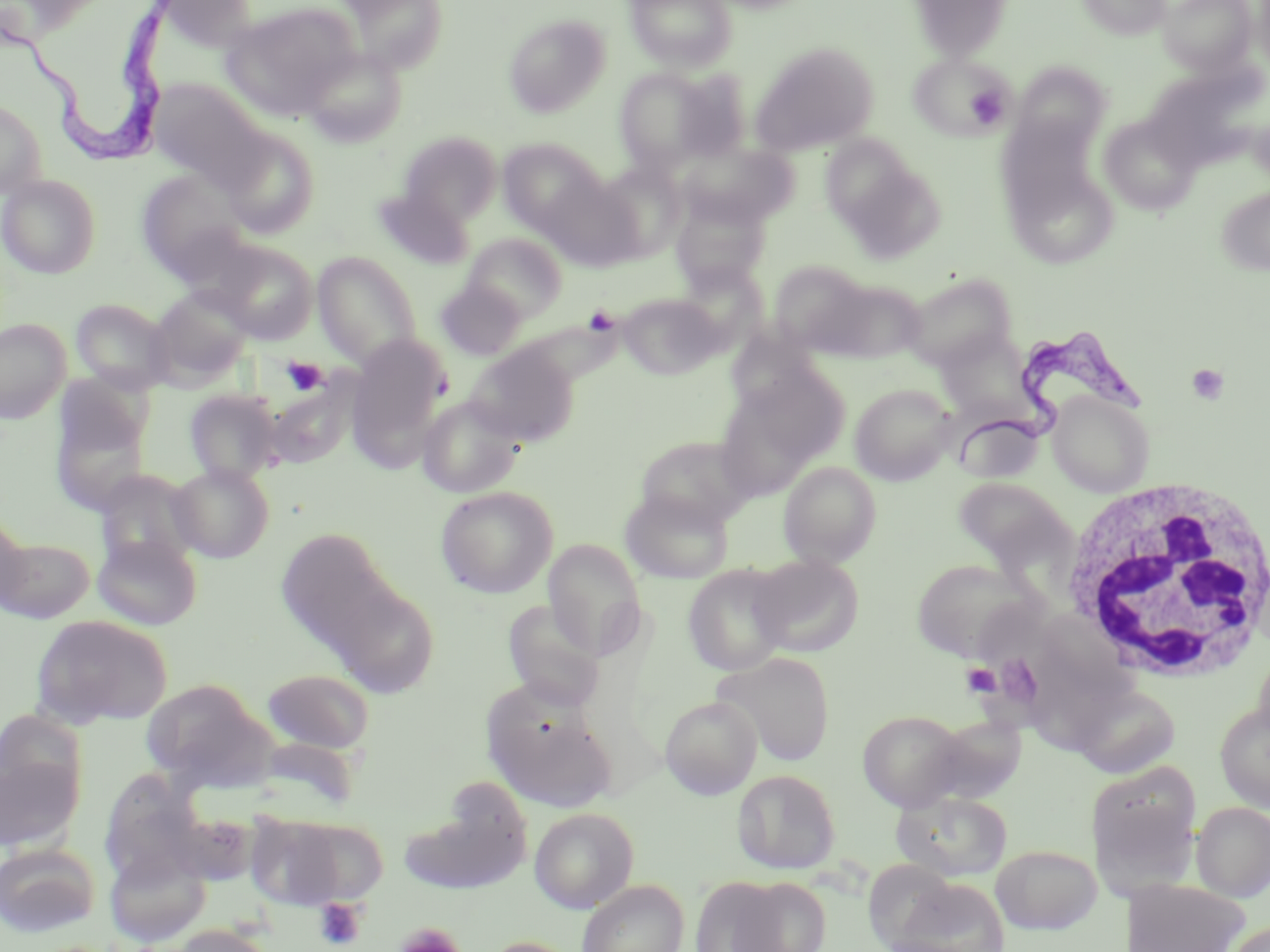

{
  "slide_level_diagnosis": "Trypanosoma brucei",
  "image_size": "1270×952 pixels",
  "trypanosoma_brucei_locations": "approximate bounding boxes as named x1/y1/x2/y2 corners in pixels: (x1=0, y1=1, x2=177, y2=155), (x1=956, y1=328, x2=1147, y2=465)",
  "modality": "optical microscopy",
  "preparation": "thin blood smear",
  "platelet_locations": "approximate bounding boxes as named x1/y1/x2/y2 corners in pixels: (x1=965, y1=85, x2=1007, y2=128), (x1=282, y1=357, x2=328, y2=395), (x1=1186, y1=363, x2=1229, y2=405), (x1=961, y1=663, x2=1000, y2=697), (x1=313, y1=898, x2=367, y2=950), (x1=397, y1=923, x2=463, y2=952)",
  "uninfected_red_blood_cell_locations": "approximate bounding boxes as named x1/y1/x2/y2 corners in pixels: (x1=150, y1=0, x2=258, y2=48), (x1=343, y1=0, x2=449, y2=73), (x1=624, y1=0, x2=738, y2=71), (x1=909, y1=0, x2=1014, y2=61), (x1=1077, y1=0, x2=1171, y2=39), (x1=1159, y1=0, x2=1256, y2=75), (x1=1252, y1=0, x2=1270, y2=76), (x1=221, y1=2, x2=360, y2=120), (x1=504, y1=15, x2=610, y2=117), (x1=751, y1=41, x2=880, y2=155), (x1=301, y1=48, x2=407, y2=147), (x1=911, y1=53, x2=1012, y2=139), (x1=1012, y1=62, x2=1113, y2=154), (x1=614, y1=68, x2=721, y2=173), (x1=671, y1=69, x2=753, y2=162), (x1=148, y1=78, x2=269, y2=187), (x1=0, y1=97, x2=47, y2=199), (x1=1099, y1=114, x2=1202, y2=216), (x1=1250, y1=115, x2=1270, y2=183), (x1=994, y1=116, x2=1108, y2=230), (x1=219, y1=129, x2=320, y2=238), (x1=399, y1=131, x2=502, y2=226), (x1=819, y1=134, x2=923, y2=233), (x1=497, y1=138, x2=605, y2=234), (x1=677, y1=141, x2=796, y2=229), (x1=595, y1=160, x2=688, y2=260), (x1=135, y1=169, x2=251, y2=279), (x1=0, y1=174, x2=101, y2=279), (x1=540, y1=175, x2=643, y2=271), (x1=1014, y1=181, x2=1117, y2=272), (x1=1216, y1=185, x2=1270, y2=275), (x1=373, y1=187, x2=473, y2=270), (x1=671, y1=194, x2=769, y2=292), (x1=463, y1=233, x2=567, y2=322), (x1=211, y1=240, x2=318, y2=343), (x1=313, y1=251, x2=424, y2=369), (x1=768, y1=260, x2=871, y2=355), (x1=902, y1=270, x2=1018, y2=370), (x1=818, y1=277, x2=926, y2=365), (x1=435, y1=279, x2=526, y2=361), (x1=149, y1=287, x2=253, y2=385), (x1=618, y1=292, x2=723, y2=380), (x1=70, y1=298, x2=175, y2=394), (x1=0, y1=318, x2=70, y2=424), (x1=345, y1=338, x2=452, y2=468), (x1=466, y1=345, x2=577, y2=447), (x1=716, y1=368, x2=847, y2=495), (x1=850, y1=383, x2=957, y2=484), (x1=49, y1=384, x2=153, y2=517), (x1=184, y1=389, x2=283, y2=484), (x1=1047, y1=391, x2=1154, y2=496), (x1=417, y1=395, x2=524, y2=498), (x1=953, y1=413, x2=1045, y2=483), (x1=634, y1=434, x2=757, y2=530), (x1=779, y1=461, x2=881, y2=568), (x1=169, y1=463, x2=275, y2=563), (x1=96, y1=471, x2=204, y2=568), (x1=952, y1=477, x2=1071, y2=571), (x1=435, y1=485, x2=558, y2=599), (x1=620, y1=489, x2=733, y2=584), (x1=0, y1=513, x2=28, y2=612), (x1=274, y1=528, x2=401, y2=659), (x1=93, y1=533, x2=203, y2=631), (x1=0, y1=535, x2=95, y2=624), (x1=543, y1=539, x2=646, y2=660), (x1=749, y1=553, x2=864, y2=657), (x1=911, y1=557, x2=1042, y2=662), (x1=683, y1=564, x2=792, y2=676), (x1=329, y1=580, x2=439, y2=697), (x1=502, y1=601, x2=606, y2=711), (x1=30, y1=614, x2=173, y2=729), (x1=1034, y1=645, x2=1120, y2=746), (x1=714, y1=652, x2=836, y2=766), (x1=261, y1=668, x2=376, y2=755), (x1=141, y1=678, x2=270, y2=788), (x1=1073, y1=684, x2=1181, y2=779), (x1=481, y1=692, x2=617, y2=815), (x1=660, y1=695, x2=762, y2=799), (x1=1215, y1=702, x2=1270, y2=811), (x1=857, y1=709, x2=969, y2=810), (x1=0, y1=711, x2=87, y2=811), (x1=928, y1=715, x2=1028, y2=805), (x1=0, y1=754, x2=81, y2=852), (x1=1087, y1=764, x2=1201, y2=893), (x1=732, y1=769, x2=841, y2=875), (x1=401, y1=785, x2=532, y2=894), (x1=892, y1=790, x2=1013, y2=881), (x1=1191, y1=801, x2=1270, y2=902), (x1=529, y1=807, x2=639, y2=912), (x1=244, y1=813, x2=352, y2=910), (x1=287, y1=817, x2=389, y2=903), (x1=0, y1=842, x2=100, y2=937), (x1=991, y1=844, x2=1101, y2=934), (x1=105, y1=847, x2=211, y2=946), (x1=888, y1=876, x2=1011, y2=952), (x1=1123, y1=877, x2=1249, y2=952), (x1=576, y1=879, x2=689, y2=952), (x1=689, y1=880, x2=801, y2=952), (x1=1223, y1=921, x2=1270, y2=952), (x1=168, y1=924, x2=276, y2=952), (x1=478, y1=936, x2=583, y2=952)",
  "magnification": "1000x",
  "stain": "May-Grünwald-Giemsa",
  "white_blood_cell_locations": "approximate bounding boxes as named x1/y1/x2/y2 corners in pixels: (x1=1055, y1=475, x2=1270, y2=685)",
  "field_of_view": "one of a larger specimen"
}